Name the parasite shown.
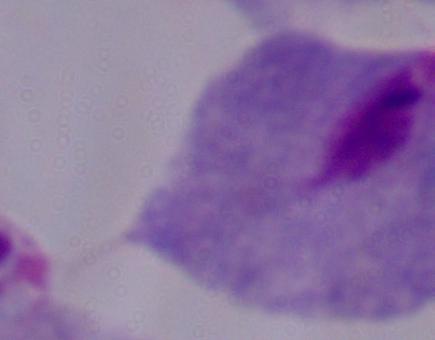

A trichomonad.

1000x magnification. Photomicrograph.